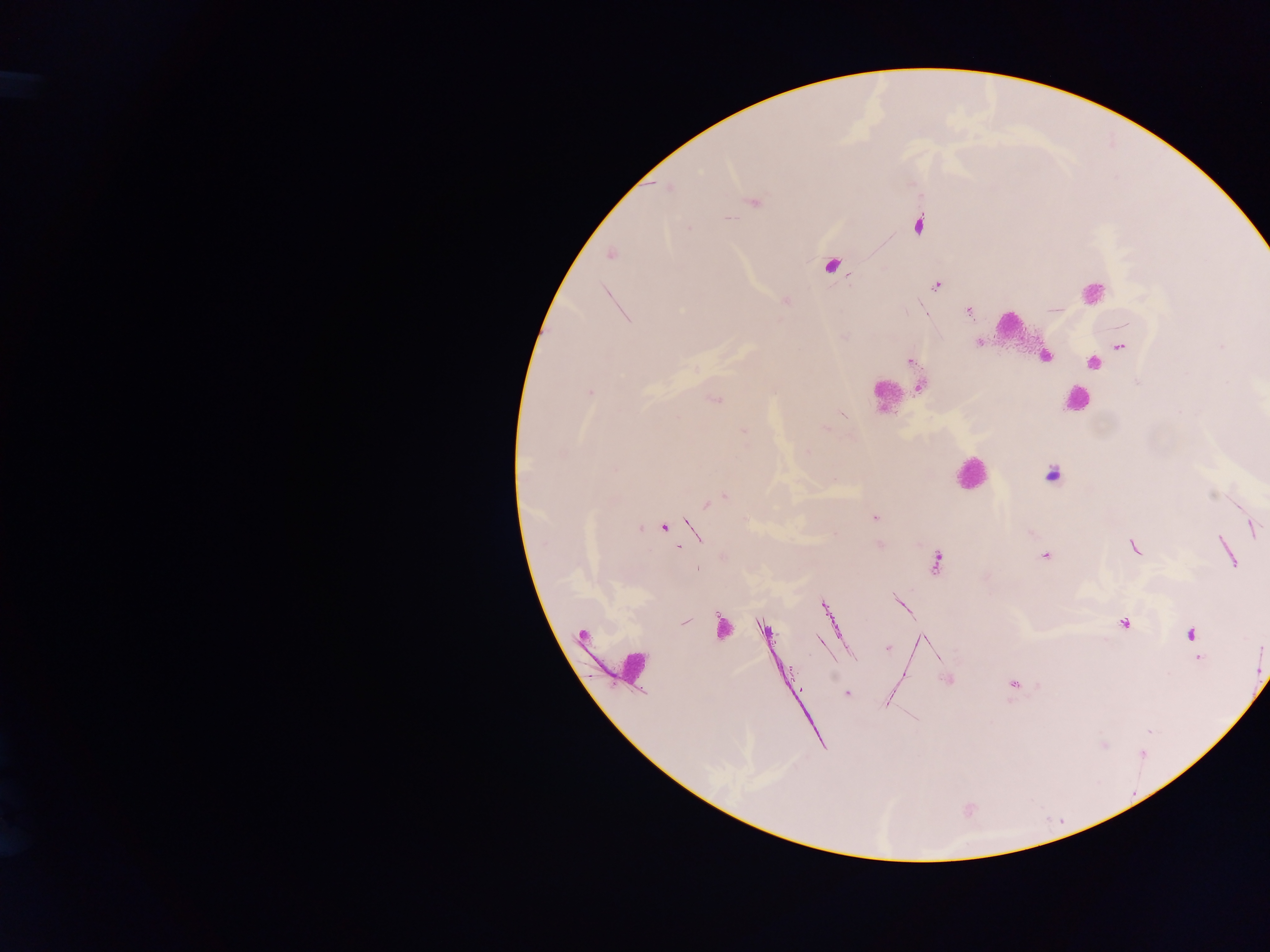
field_of_view: single
capture: mobile-phone photograph through a microscope
leukocyte_locations: 'approximate centers as x y in pixels: 1092 291; 1010 329; 886 395; 1076 401; 969 473'
country: Ghana
image_size: 1270×952 pixels
plasmodium_parasite_locations: 'approximate centers as x y in pixels: 669 188; 755 203; 918 224; 689 228; 611 254; 832 265; 936 286; 785 300; 969 310; 925 313; 979 342; 1222 346; 1121 347; 1045 356; 910 361; 1094 363; 1138 382; 920 387; 590 392; 715 400; 842 414; 826 428; 744 431; 808 452; 1052 475; 725 497; 708 503; 874 517; 664 528; 1254 528; 1133 547; 1045 556; 937 563; 901 603; 823 605; 684 622; 1124 623; 721 627; 765 630; 1191 636; 820 641; 888 648; 1198 658; 948 680; 1013 684; 847 693; 887 703'
preparation: thick blood film